Locate every blood parasite and identify its species.
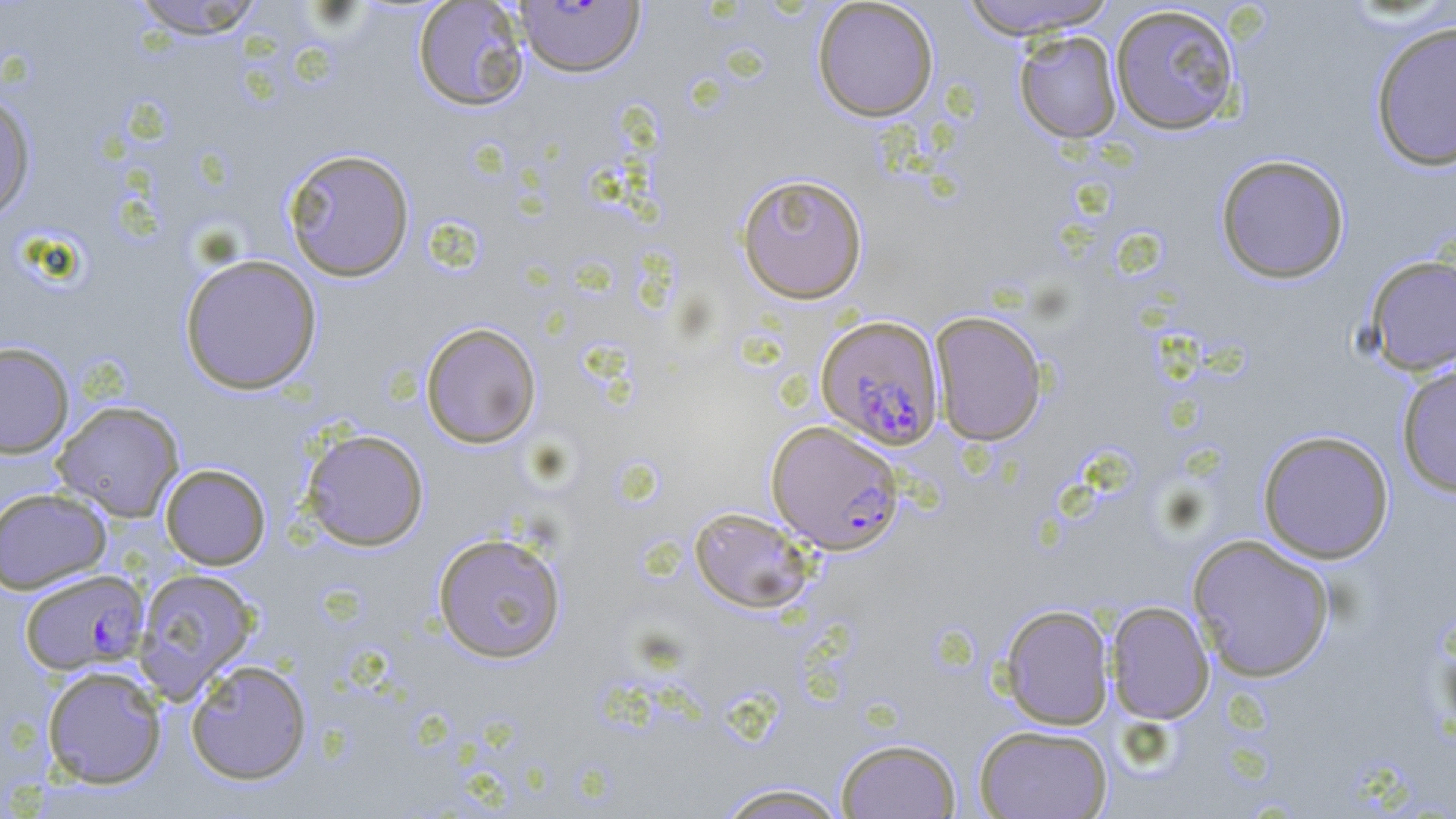
Approximate bounding boxes as [x1, y1, x2, y2] in pixels.
Plasmodium falciparum-infected red blood cells: [514, 1, 646, 79], [815, 315, 944, 449], [766, 420, 904, 553], [19, 569, 149, 674].
No Plasmodium ovale, Plasmodium malariae, Plasmodium vivax, Babesia divergens, or Trypanosoma brucei observed.

Uninfected red blood cell locations: [129, 0, 268, 39], [957, 0, 1120, 38], [412, 1, 530, 112], [811, 1, 939, 122], [1109, 4, 1242, 135], [1369, 19, 1456, 172], [1014, 31, 1122, 143], [0, 91, 37, 221], [282, 147, 416, 282], [1215, 154, 1350, 283], [735, 172, 869, 304], [179, 253, 322, 395], [1363, 253, 1456, 376], [929, 311, 1048, 446], [420, 322, 542, 449], [0, 341, 74, 457], [1395, 361, 1456, 497], [52, 401, 185, 521], [300, 428, 430, 551], [1257, 429, 1394, 563], [160, 463, 270, 569], [0, 487, 112, 594], [689, 506, 815, 613], [432, 531, 568, 664], [1187, 533, 1336, 682], [133, 567, 260, 700], [1106, 601, 1215, 724], [999, 604, 1114, 730], [185, 659, 312, 784], [41, 664, 167, 789], [974, 724, 1112, 819], [835, 738, 962, 818], [715, 782, 851, 819]. Slide-level diagnosis: Plasmodium falciparum. Image is 1456×819 pixels. 1000x magnification. May-Grünwald-Giemsa stain. One field of a larger specimen. Optical microscopy. Thin blood smear.